Name the parasite shown.
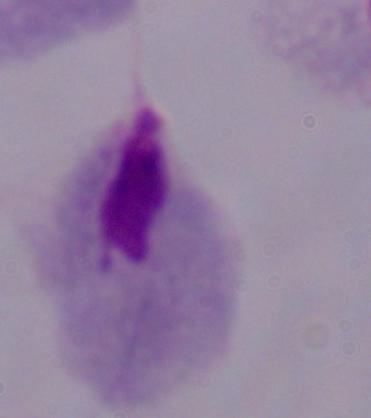
A trichomonad.

Photomicrograph. 1000x magnification.